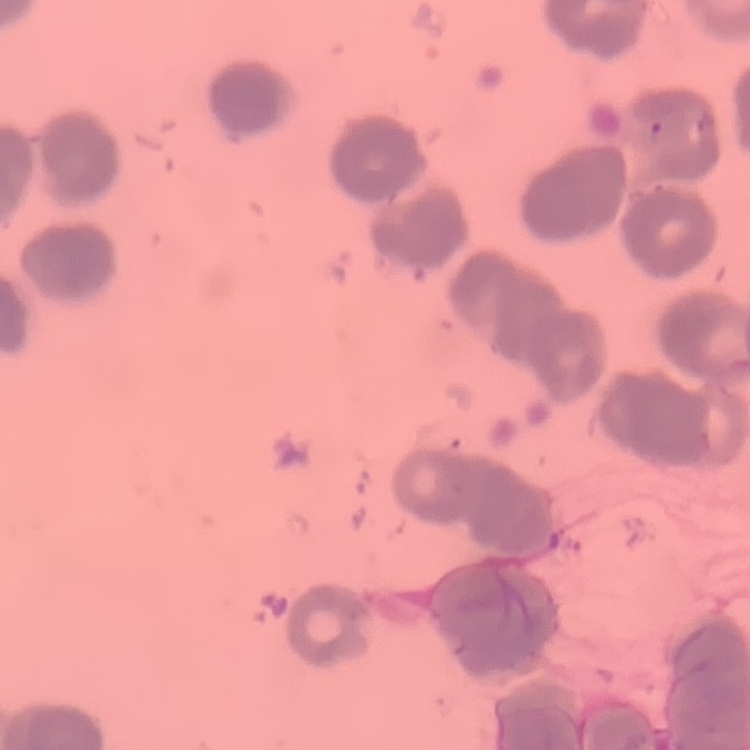 The red blood cells show rouleaux formation. Thin blood film. Stained with either Field's or Giemsa. One tile cut from a larger photomicrograph.